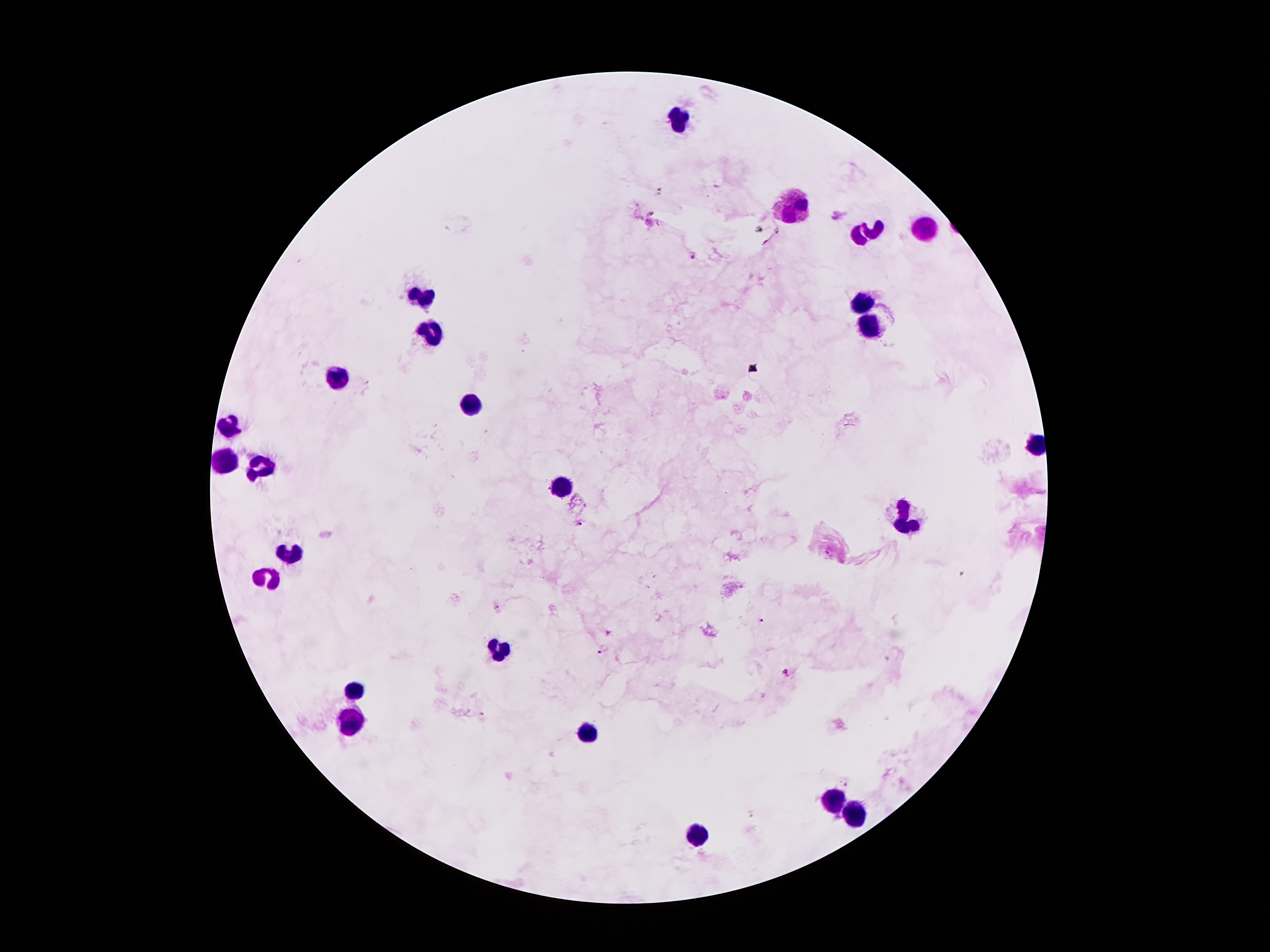

Approximate centers as [x, y] in pixels.
Summary:
  - Leukocyte locations: [679, 124], [796, 212], [927, 230], [865, 234], [425, 291], [867, 302], [874, 326], [431, 327], [343, 378], [470, 405], [232, 425], [230, 461], [261, 466], [562, 485], [906, 519], [290, 547], [267, 578], [501, 646], [357, 691], [351, 717], [587, 734], [833, 799], [857, 814], [701, 835]
  - Malaria parasite locations: [693, 257], [581, 524], [496, 607], [760, 621], [607, 631], [602, 651], [785, 672], [846, 784], [751, 815]
  - Magnification: 100x
  - Preparation: thick blood smear
  - Patient malaria status: positive for Plasmodium falciparum
  - Image size: 1270×952 pixels
  - Field of view: single
  - Capture: smartphone camera through the microscope eyepiece
  - Stain: Giemsa